Identify the parasite.
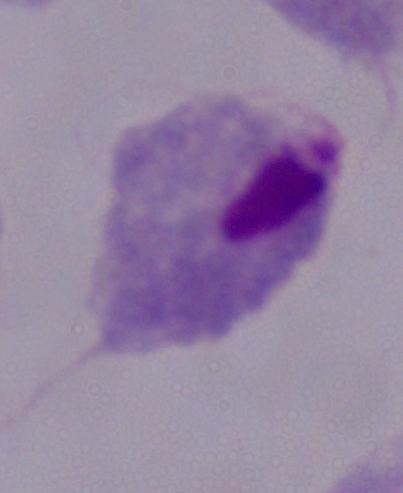

A trichomonad.

Summary:
  - Modality: micrograph
  - Magnification: 1000x